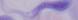
Summary:
  - Modality: photomicrograph
  - Identification: trypanosome
  - Magnification: 1000x